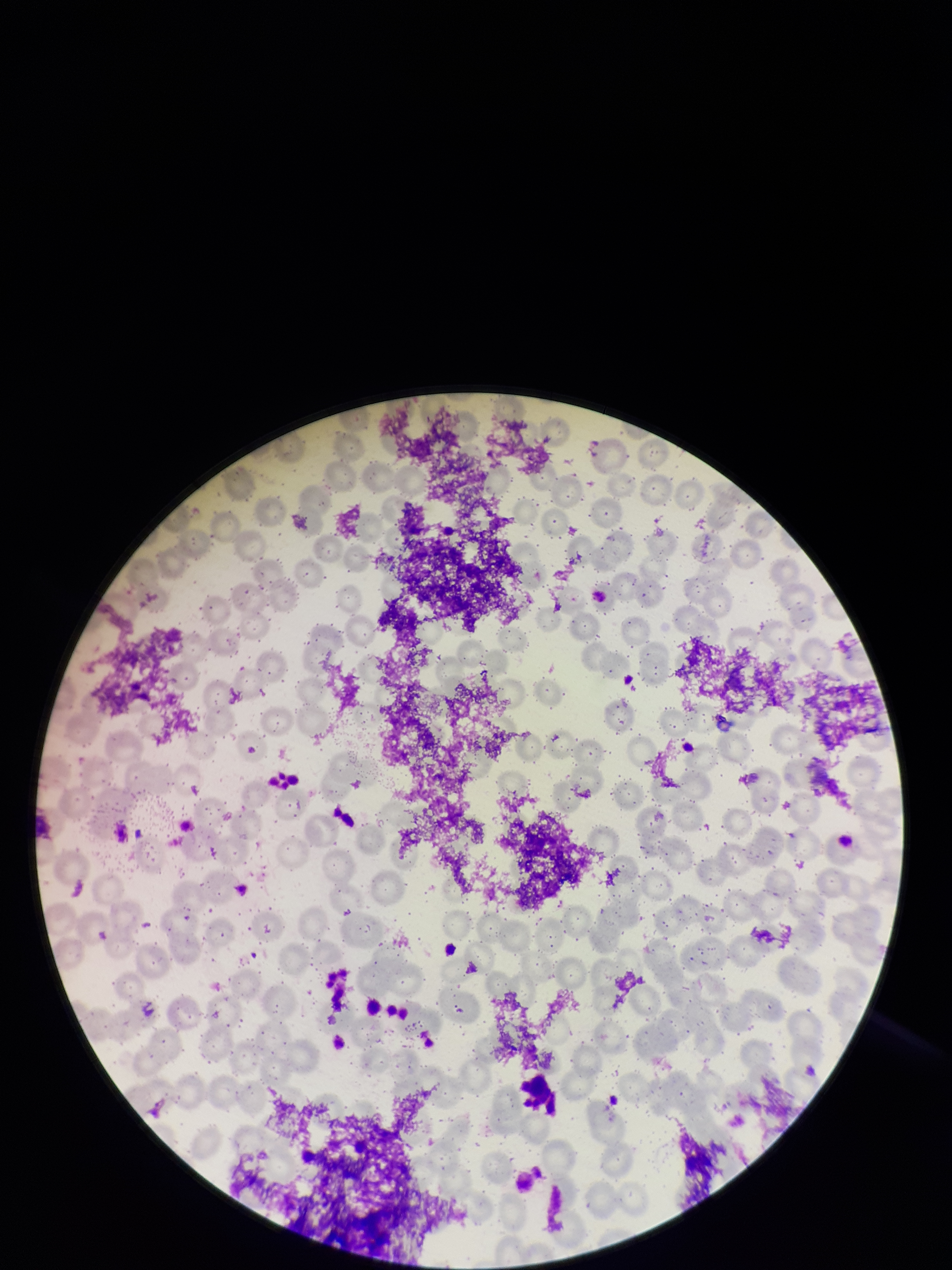

field of view = single
red blood cell count = 249
parasitized red blood cell count = 0
preparation = thin smear
parasitized red blood cells = none detected
patient malaria status = negative
capture = smartphone photograph through the microscope eyepiece
stain = Giemsa
image size = 952×1270 pixels